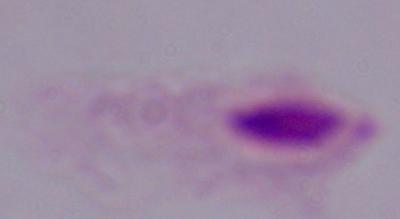 Micrograph. 1000x magnification. A trichomonad is shown.